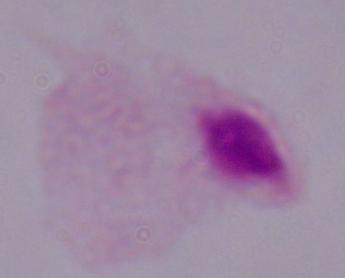
identification: trichomonad
modality: micrograph
magnification: 1000x